Report the malaria status of this cell.
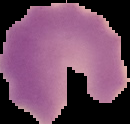

It is parasitized.

image_type: segmented cell region on a black background
image_size: 130×124 pixels
preparation: thin blood film